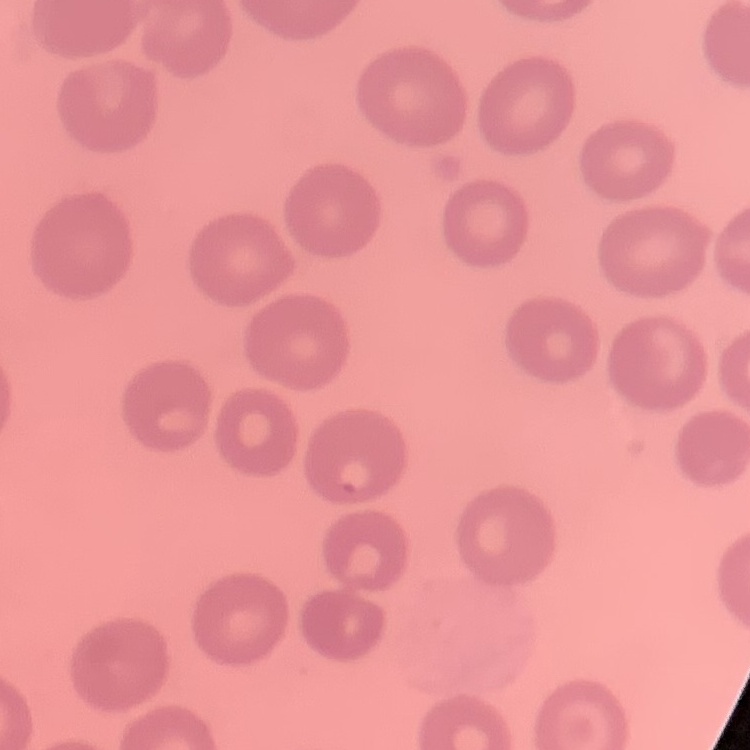

Summary:
  - Erythrocyte morphology: no rouleaux formation
  - Stain: Field's or Giemsa
  - Preparation: thin peripheral smear
  - Image type: one tile cut from a larger photomicrograph